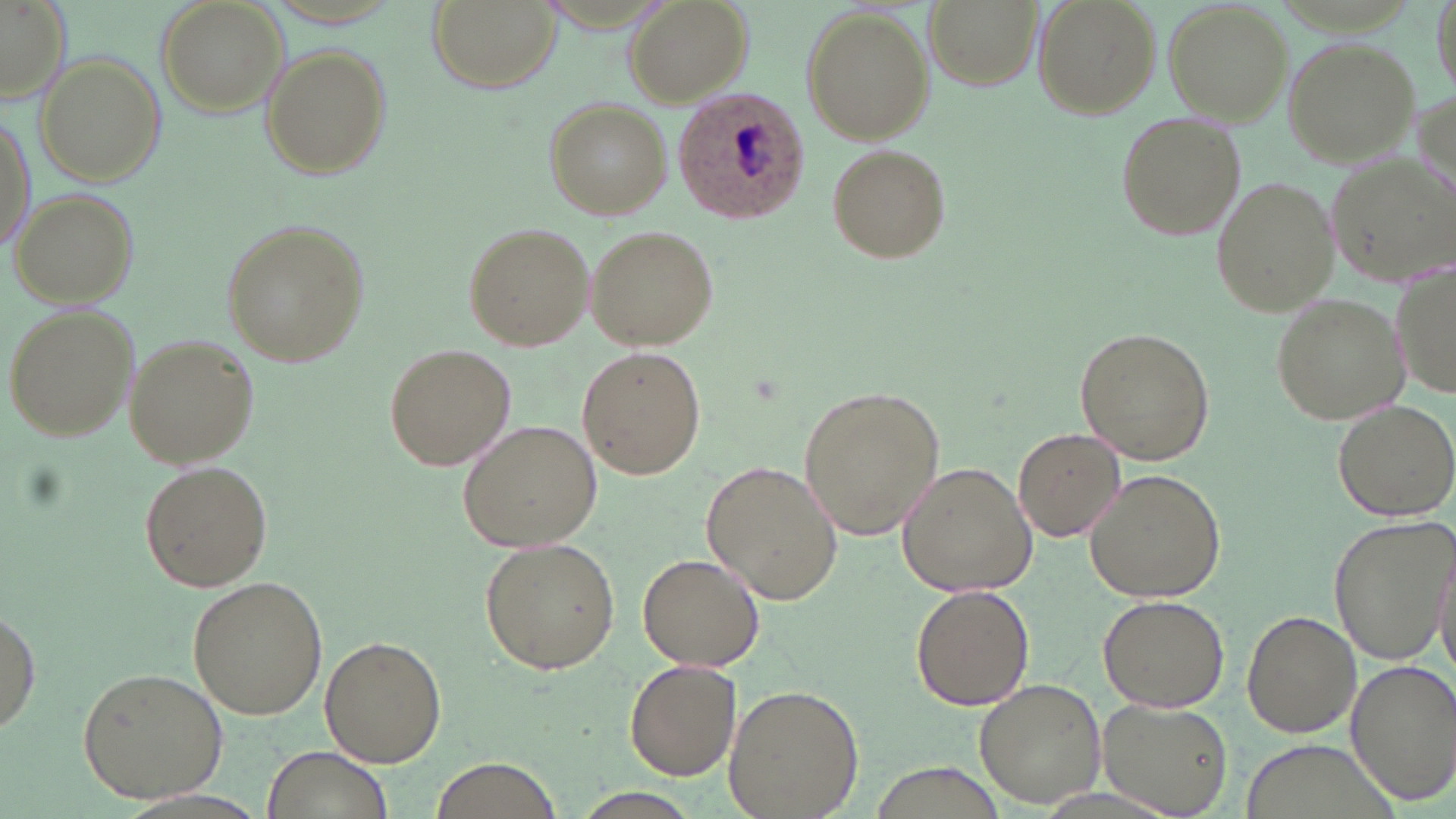

slide_level_diagnosis: Plasmodium ovale
image_size: 1456×819 pixels
field_of_view: one of a larger specimen
preparation: thin blood smear
stain: May-Grünwald-Giemsa
uninfected_red_blood_cell_locations: 'approximate bounding boxes as named x1/y1/x2/y2 corners in pixels: (x1=156, y1=0, x2=288, y2=117), (x1=428, y1=0, x2=555, y2=94), (x1=623, y1=0, x2=751, y2=107), (x1=925, y1=0, x2=1041, y2=89), (x1=1031, y1=0, x2=1159, y2=118), (x1=1431, y1=0, x2=1454, y2=101), (x1=0, y1=2, x2=72, y2=103), (x1=1163, y1=2, x2=1291, y2=125), (x1=800, y1=7, x2=934, y2=143), (x1=1284, y1=38, x2=1420, y2=168), (x1=260, y1=45, x2=390, y2=180), (x1=35, y1=52, x2=164, y2=187), (x1=1412, y1=89, x2=1454, y2=204), (x1=544, y1=97, x2=670, y2=218), (x1=1, y1=107, x2=35, y2=257), (x1=1113, y1=110, x2=1246, y2=242), (x1=825, y1=142, x2=953, y2=262), (x1=1327, y1=155, x2=1454, y2=287), (x1=1210, y1=177, x2=1339, y2=318), (x1=10, y1=188, x2=141, y2=308), (x1=220, y1=217, x2=371, y2=370), (x1=462, y1=221, x2=595, y2=351), (x1=583, y1=225, x2=720, y2=350), (x1=1390, y1=261, x2=1455, y2=404), (x1=1270, y1=292, x2=1407, y2=426), (x1=3, y1=303, x2=139, y2=444), (x1=1075, y1=326, x2=1215, y2=467), (x1=123, y1=333, x2=259, y2=469), (x1=382, y1=343, x2=516, y2=469), (x1=577, y1=345, x2=706, y2=479), (x1=797, y1=383, x2=946, y2=543), (x1=1331, y1=400, x2=1456, y2=521), (x1=457, y1=417, x2=602, y2=549), (x1=1014, y1=427, x2=1124, y2=542), (x1=702, y1=458, x2=845, y2=606), (x1=138, y1=459, x2=273, y2=593), (x1=897, y1=463, x2=1036, y2=597), (x1=1084, y1=469, x2=1225, y2=603), (x1=1328, y1=517, x2=1453, y2=664), (x1=479, y1=538, x2=622, y2=674), (x1=1432, y1=551, x2=1456, y2=683), (x1=638, y1=553, x2=765, y2=673), (x1=187, y1=576, x2=329, y2=721), (x1=910, y1=585, x2=1033, y2=711), (x1=1097, y1=595, x2=1229, y2=713), (x1=0, y1=609, x2=41, y2=739), (x1=1243, y1=610, x2=1360, y2=738), (x1=320, y1=635, x2=446, y2=768), (x1=1345, y1=658, x2=1455, y2=806), (x1=626, y1=659, x2=741, y2=782), (x1=76, y1=667, x2=228, y2=803), (x1=975, y1=680, x2=1107, y2=808), (x1=722, y1=683, x2=865, y2=819), (x1=1096, y1=699, x2=1233, y2=818), (x1=1240, y1=739, x2=1398, y2=818), (x1=260, y1=745, x2=396, y2=819), (x1=434, y1=758, x2=558, y2=818), (x1=568, y1=790, x2=702, y2=819)'
magnification: 1000x
plasmodium_ovale_infected_red_blood_cell_locations: 'approximate bounding boxes as named x1/y1/x2/y2 corners in pixels: (x1=674, y1=88, x2=811, y2=221)'
modality: light microscopy